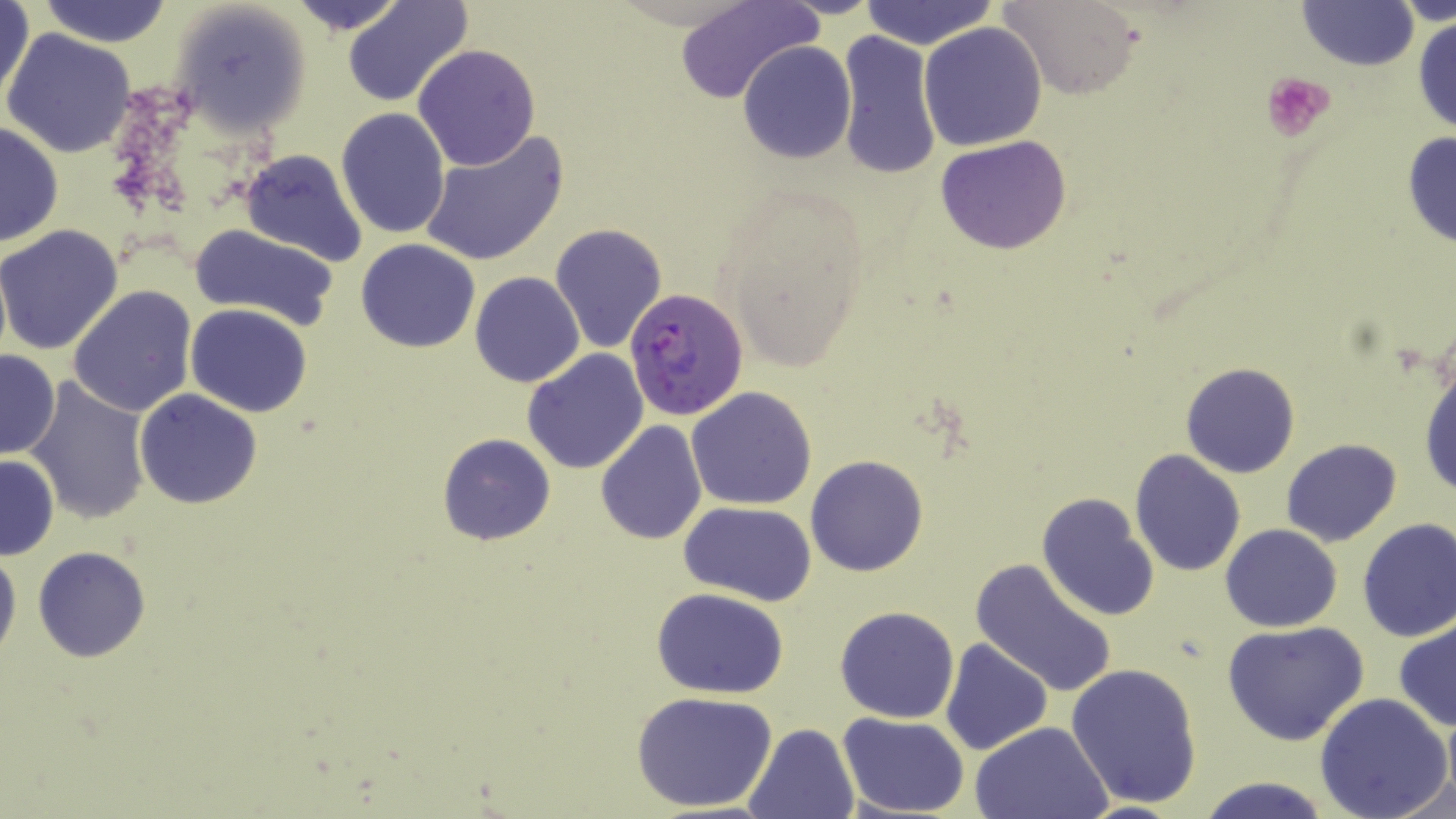
Summary:
  - Coordinate format: approximate bounding boxes as (x1, y1, x2, y2) in pixels
  - Platelet locations: (1260, 71, 1337, 143)
  - Plasmodium falciparum-infected red blood cell locations: (624, 286, 749, 421)
  - Uninfected red blood cell locations: (1, 0, 34, 108), (36, 0, 175, 46), (284, 0, 411, 35), (339, 0, 472, 108), (859, 0, 999, 50), (1003, 0, 1143, 100), (1391, 0, 1456, 25), (170, 1, 311, 137), (673, 1, 819, 106), (1297, 1, 1417, 73), (1412, 13, 1456, 137), (918, 22, 1047, 152), (3, 30, 134, 159), (835, 31, 942, 181), (737, 41, 856, 164), (412, 44, 542, 172), (336, 107, 451, 238), (0, 121, 63, 248), (416, 129, 570, 269), (1401, 131, 1456, 252), (937, 134, 1071, 255), (238, 148, 368, 265), (548, 222, 667, 356), (188, 223, 341, 330), (0, 224, 125, 357), (355, 239, 481, 353), (469, 273, 585, 388), (67, 285, 197, 417), (185, 303, 314, 418), (0, 348, 61, 460), (522, 348, 650, 475), (1418, 361, 1455, 500), (1180, 362, 1300, 478), (24, 381, 151, 526), (686, 386, 817, 510), (135, 388, 264, 510), (594, 420, 707, 545), (437, 433, 556, 546), (1281, 438, 1401, 545), (1131, 449, 1247, 577), (1, 453, 59, 560), (806, 454, 928, 576), (1037, 492, 1160, 623), (679, 500, 816, 605), (1355, 517, 1456, 642), (1222, 525, 1342, 631), (0, 544, 21, 670), (32, 546, 154, 663), (970, 557, 1120, 699), (650, 587, 790, 697), (834, 606, 961, 723), (1394, 616, 1456, 732), (1222, 620, 1370, 746), (940, 637, 1052, 755), (1066, 661, 1203, 807), (632, 691, 776, 812), (1314, 692, 1451, 819), (1441, 711, 1455, 804), (838, 712, 969, 817), (971, 720, 1115, 819), (743, 722, 858, 819), (1387, 768, 1456, 819), (1195, 776, 1331, 819)
  - Slide-level diagnosis: Plasmodium falciparum
  - Preparation: thin blood film
  - Magnification: 1000x
  - Modality: light microscopy
  - Stain: May-Grünwald-Giemsa
  - Image size: 1456×819 pixels
  - Field of view: single